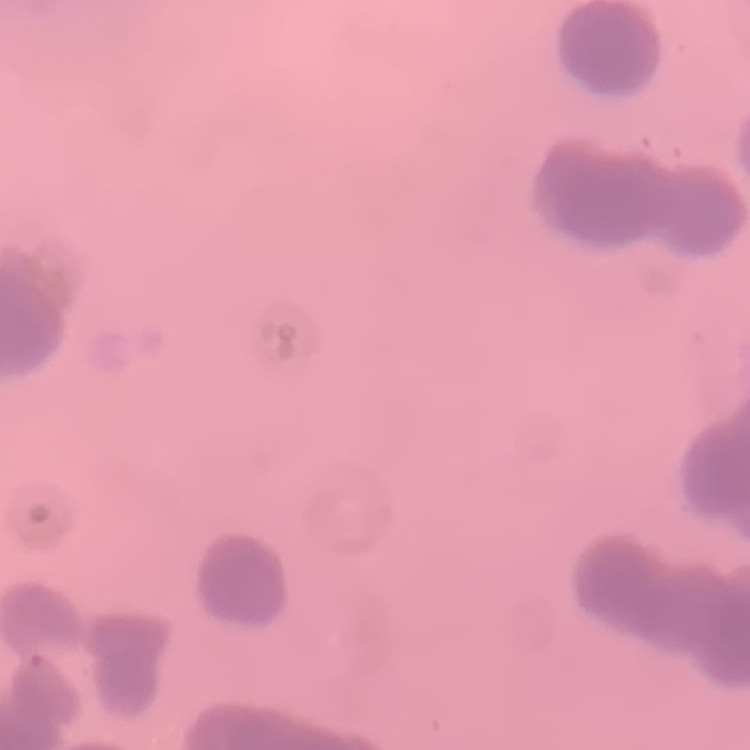

red blood cell morphology = rouleaux formation
image type = one tile cut from a larger photomicrograph
preparation = thin peripheral smear
stain = Field's or Giemsa